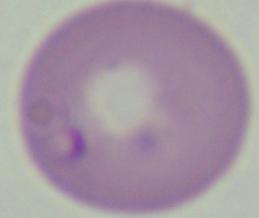

magnification = 1000x
modality = micrograph
identification = Babesia